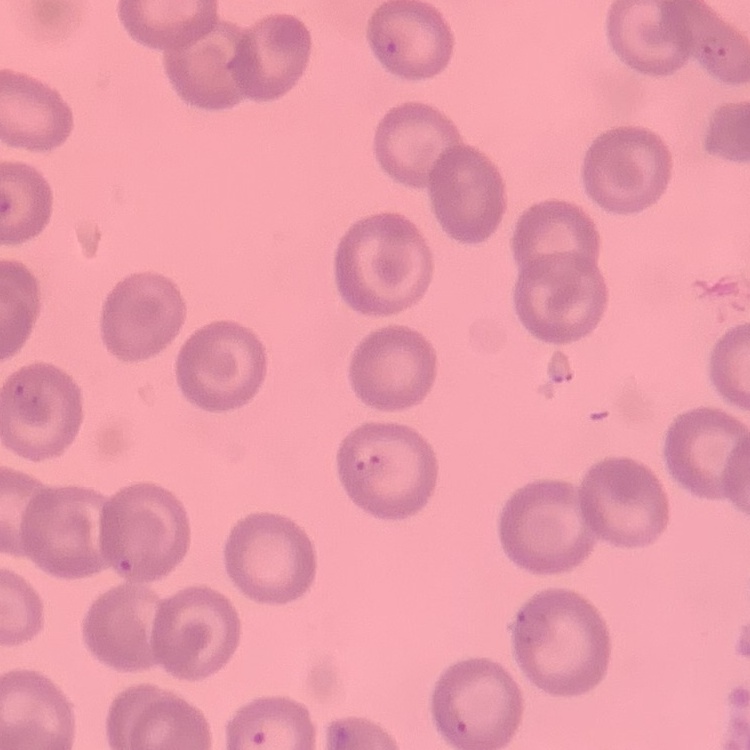
Summary:
  - Red blood cell morphology: no rouleaux formation
  - Preparation: thin blood smear
  - Image type: one tile cut from a larger photomicrograph
  - Stain: Field's or Giemsa